Outline each blood parasite and name the species.
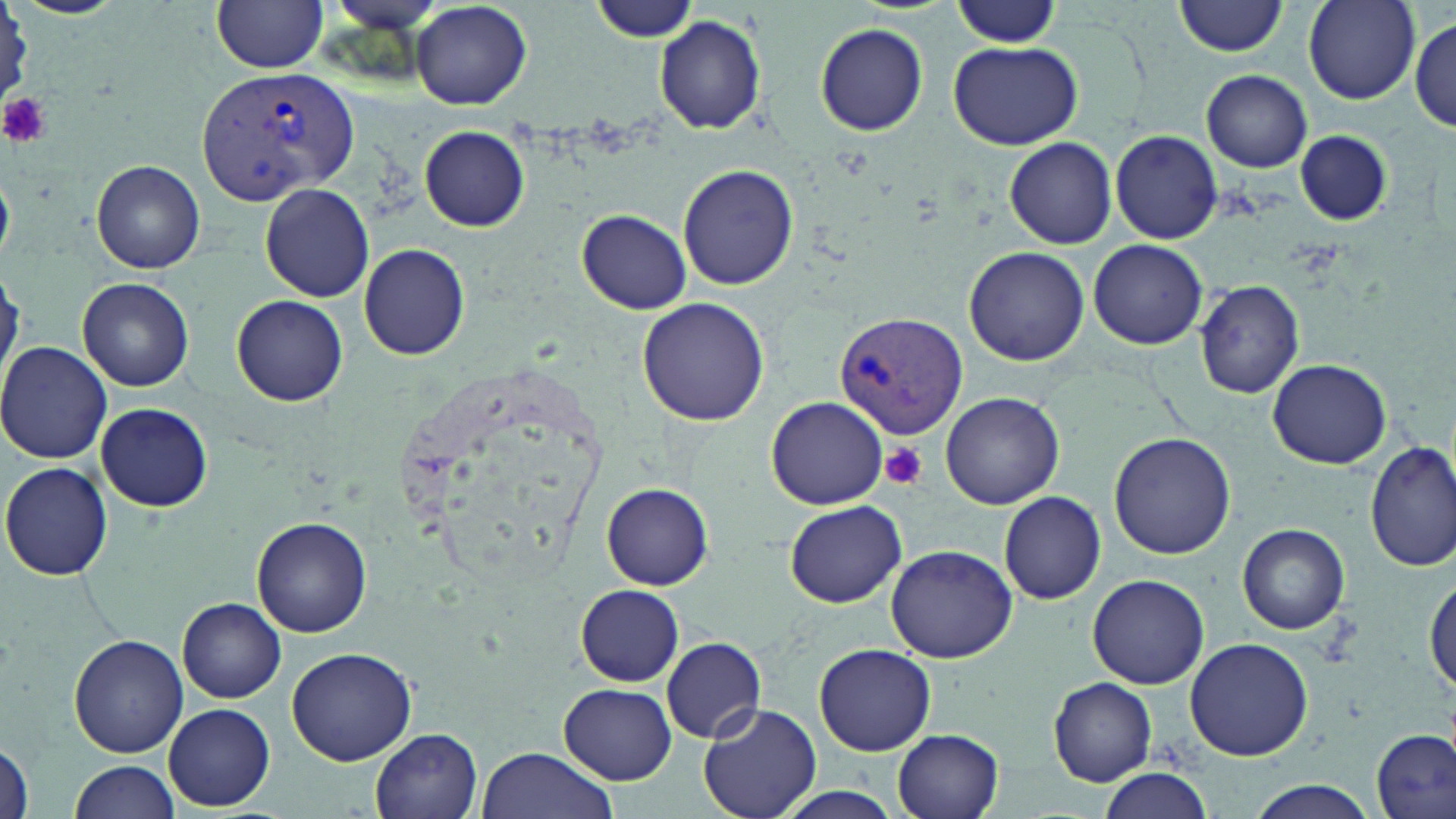
Approximate bounding boxes as [x1, y1, x2, y2] in pixels.
Plasmodium vivax-infected red blood cells: [196, 65, 358, 206], [835, 312, 967, 438].
No Plasmodium falciparum, Plasmodium ovale, Plasmodium malariae, Babesia divergens, or Trypanosoma brucei observed.

Summary:
  - Platelet locations: [0, 93, 51, 149], [881, 442, 926, 489]
  - Uninfected red blood cell locations: [212, 0, 329, 73], [1176, 0, 1289, 57], [411, 1, 531, 110], [588, 1, 700, 44], [945, 1, 1064, 48], [1303, 1, 1419, 104], [655, 15, 766, 135], [1410, 16, 1456, 130], [815, 24, 928, 135], [947, 39, 1083, 150], [1201, 70, 1313, 173], [420, 125, 529, 232], [1296, 130, 1391, 227], [1110, 131, 1223, 244], [1005, 138, 1118, 249], [92, 160, 205, 274], [678, 165, 799, 291], [0, 172, 13, 263], [261, 183, 374, 302], [576, 209, 692, 314], [1088, 238, 1209, 350], [360, 245, 469, 360], [963, 247, 1090, 366], [0, 269, 20, 390], [78, 277, 193, 391], [1195, 280, 1305, 398], [232, 293, 349, 406], [637, 298, 771, 426], [0, 342, 115, 464], [1268, 358, 1391, 468], [940, 392, 1065, 510], [766, 396, 888, 510], [94, 402, 213, 513], [1109, 431, 1236, 559], [1366, 440, 1456, 573], [2, 461, 114, 580], [602, 482, 714, 589], [998, 491, 1105, 604], [784, 499, 908, 606], [253, 517, 373, 639], [1237, 523, 1350, 635], [885, 544, 1018, 663], [1087, 573, 1210, 688], [1426, 575, 1456, 700], [575, 584, 685, 686], [178, 597, 286, 703], [68, 634, 187, 757], [661, 637, 766, 744], [1183, 638, 1314, 760], [813, 645, 936, 756], [286, 646, 418, 766], [1049, 677, 1157, 785], [559, 683, 677, 783], [164, 703, 274, 811], [699, 703, 821, 819], [1372, 728, 1454, 819], [371, 729, 484, 818], [893, 729, 1003, 819], [0, 742, 33, 819], [474, 747, 621, 819], [69, 759, 180, 818], [1094, 767, 1213, 818], [1243, 781, 1379, 818]
  - Slide-level diagnosis: Plasmodium vivax
  - Image size: 1456×819 pixels
  - Modality: optical microscopy
  - Field of view: single
  - Preparation: thin blood film
  - Magnification: 1000x
  - Stain: May-Grünwald-Giemsa